Give the extent of all Babesia divergens-infected red blood cells.
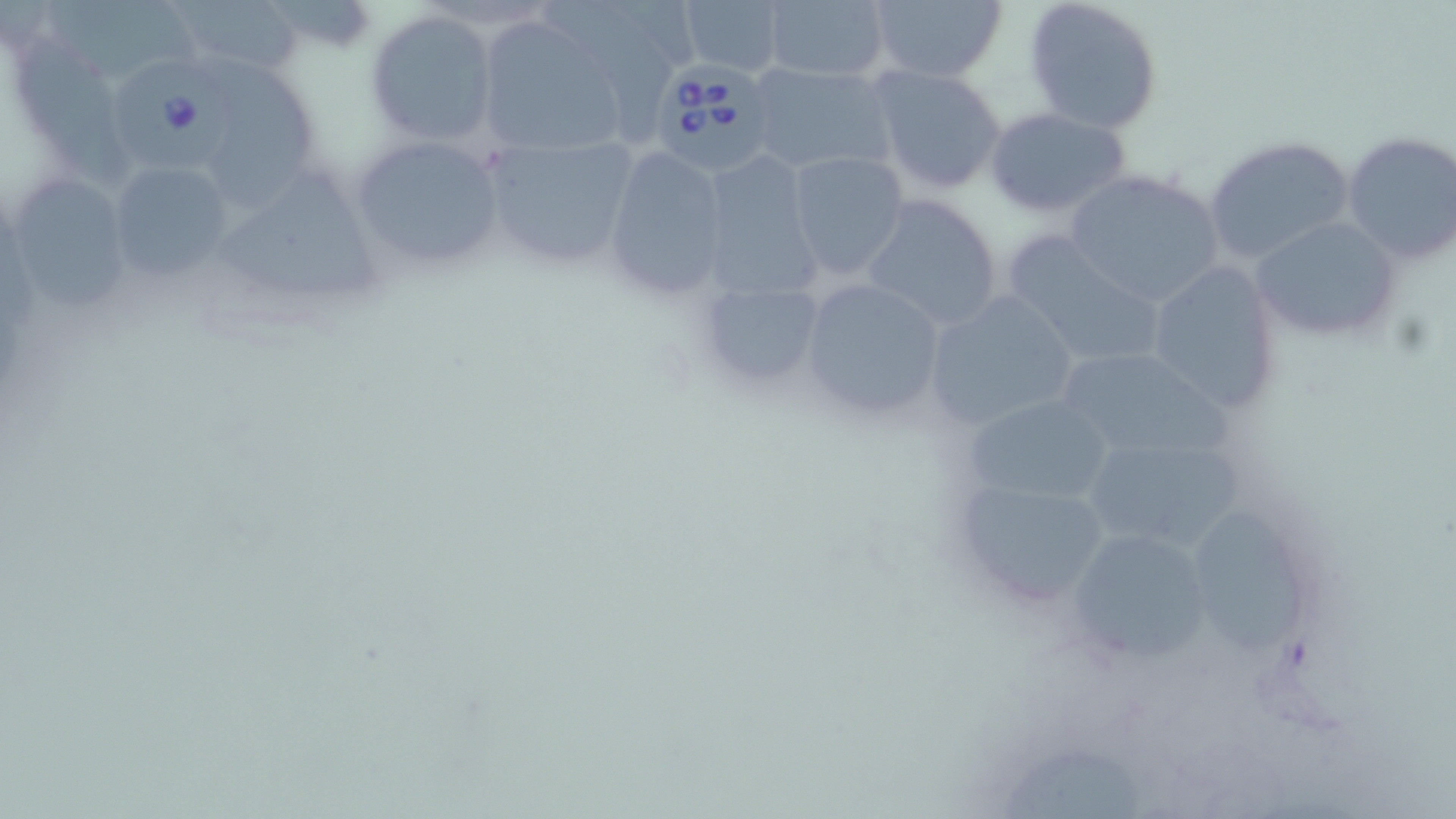
Approximate bounding boxes as (x1, y1, x2, y2) in pixels.
Babesia divergens-infected red blood cells: (649, 49, 775, 178), (118, 63, 246, 176).

slide_level_diagnosis: Babesia divergens
preparation: thin blood smear
modality: optical microscopy
uninfected_red_blood_cell_locations: 'approximate bounding boxes as (x1, y1, x2, y2) in pixels: (162, 0, 306, 81), (677, 0, 787, 78), (759, 0, 893, 82), (864, 0, 1008, 84), (1022, 0, 1164, 133), (547, 1, 676, 133), (44, 3, 210, 81), (364, 9, 500, 147), (474, 16, 632, 161), (24, 34, 149, 186), (209, 51, 330, 214), (746, 62, 901, 178), (865, 63, 1007, 196), (984, 106, 1133, 219), (475, 129, 645, 274), (1339, 130, 1456, 268), (347, 133, 506, 273), (1202, 134, 1357, 266), (600, 146, 733, 300), (710, 149, 830, 303), (786, 149, 910, 281), (105, 160, 238, 280), (17, 166, 132, 310), (1062, 167, 1225, 310), (219, 174, 385, 305), (860, 194, 1004, 332), (1251, 216, 1401, 343), (999, 233, 1167, 370), (1143, 259, 1283, 413), (687, 270, 831, 402), (797, 275, 949, 423), (922, 290, 1082, 432), (1055, 346, 1226, 461), (963, 392, 1119, 512), (1092, 445, 1247, 550), (947, 472, 1114, 609), (1205, 520, 1305, 662), (1062, 526, 1220, 667)'
image_size: 1456×819 pixels
field_of_view: single
magnification: 1000x
stain: May-Grünwald-Giemsa